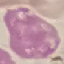
Result: no malaria parasites seen. Cell patch, automatically extracted from a larger field of view and resized to 64 × 64 pixels. Giemsa-stained preparation. Thin blood film. Photographed with a smartphone camera at the microscope eyepiece.